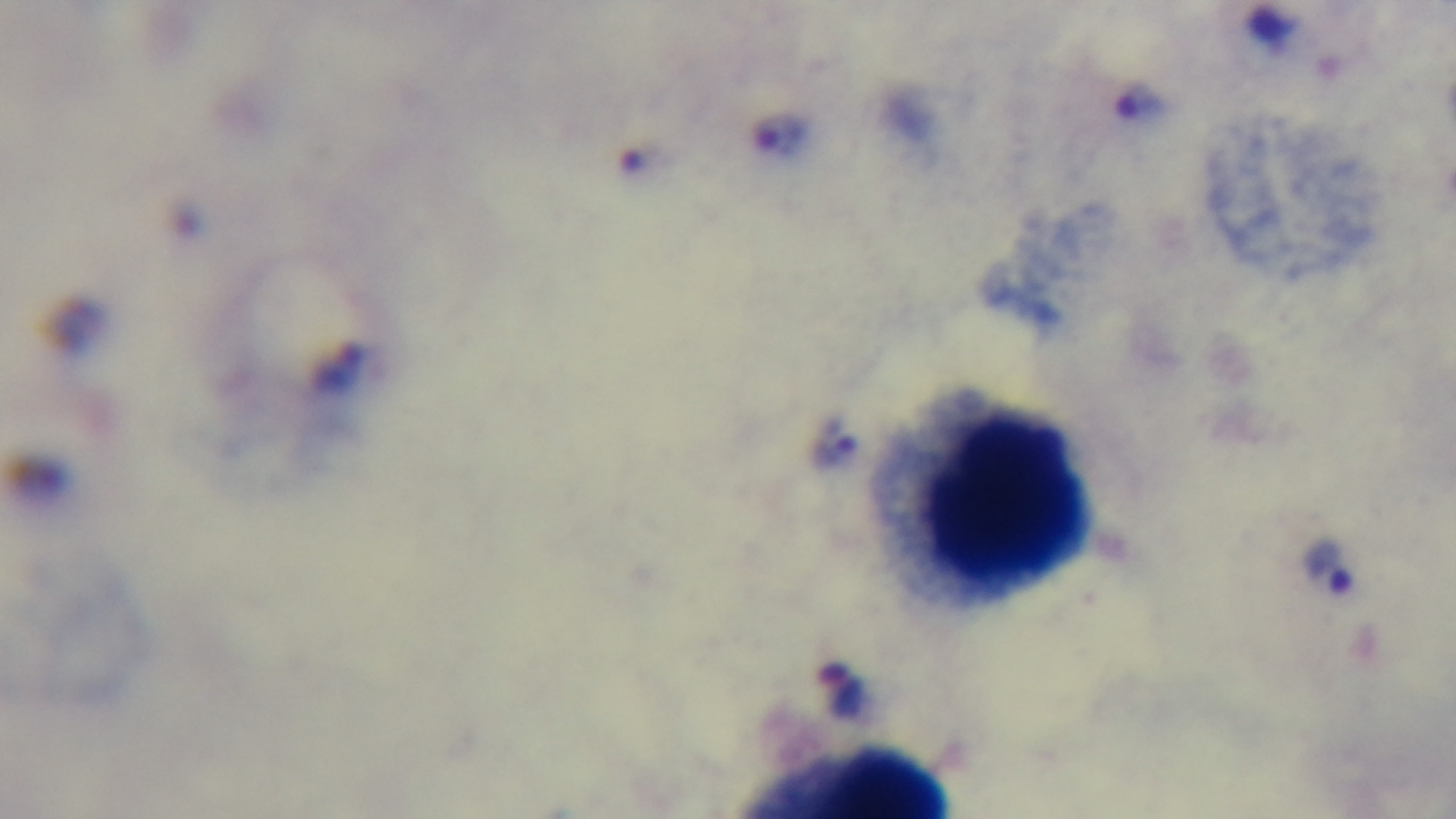

Summary:
  - Preparation: thick smear
  - Malaria status: positive
  - Capture: mounted 4K digital camera
  - Modality: light microscopy
  - Objective: 100x oil immersion
  - Stain: Giemsa
  - Field of view: single